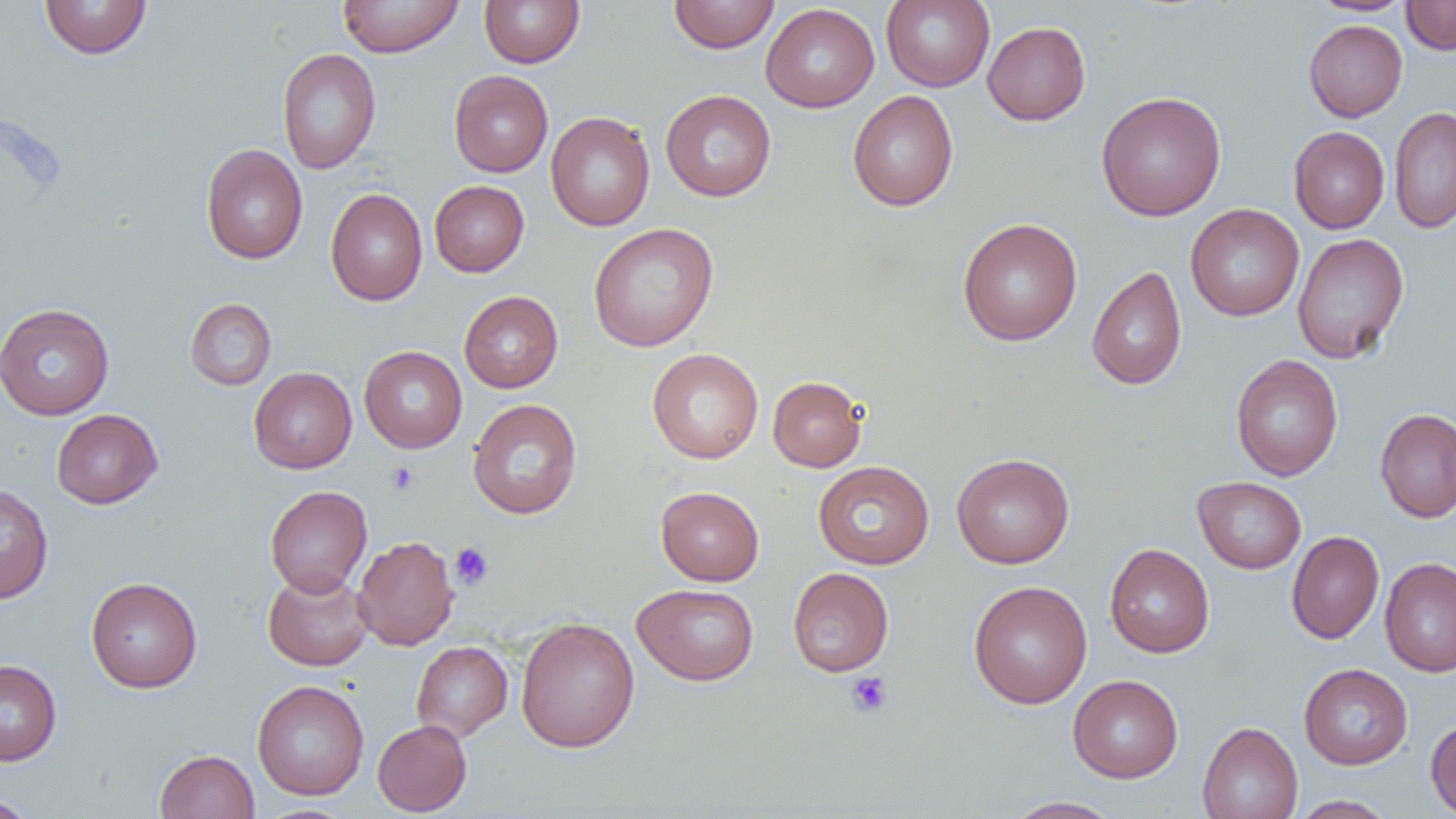

Summary:
  - Coordinate format: approximate bounding boxes as (x1, y1, x2, y2) in pixels
  - Uninfected red blood cell locations: (39, 0, 152, 59), (338, 0, 463, 57), (479, 0, 585, 68), (669, 0, 780, 53), (881, 0, 995, 91), (1308, 0, 1416, 16), (1401, 0, 1456, 55), (761, 3, 880, 112), (1303, 19, 1407, 122), (982, 21, 1091, 126), (277, 48, 381, 174), (448, 70, 553, 177), (660, 90, 776, 202), (848, 90, 959, 211), (1096, 91, 1226, 220), (1389, 106, 1456, 233), (545, 112, 655, 231), (1289, 126, 1390, 234), (201, 144, 308, 264), (429, 180, 529, 276), (325, 188, 427, 305), (1185, 204, 1304, 321), (957, 217, 1083, 346), (588, 223, 719, 352), (1292, 232, 1410, 364), (1087, 266, 1187, 390), (459, 291, 563, 393), (185, 298, 276, 390), (0, 303, 115, 420), (359, 346, 467, 453), (647, 348, 764, 463), (1230, 354, 1343, 481), (248, 367, 357, 473), (768, 375, 866, 472), (467, 398, 582, 519), (1375, 408, 1456, 523), (51, 409, 162, 509), (951, 452, 1075, 569), (813, 460, 934, 569), (1193, 476, 1306, 573), (0, 482, 54, 604), (265, 485, 372, 597), (655, 486, 764, 586), (1286, 530, 1384, 644), (352, 535, 459, 650), (1104, 543, 1214, 658), (1380, 557, 1456, 676), (787, 567, 894, 676), (262, 569, 374, 671), (85, 577, 203, 693), (968, 580, 1092, 708), (632, 583, 759, 686), (515, 617, 640, 753), (411, 641, 512, 742), (0, 659, 62, 766), (1299, 663, 1413, 769), (1068, 675, 1183, 783), (252, 680, 369, 800), (1425, 717, 1456, 818), (372, 719, 472, 816), (1197, 721, 1303, 819), (155, 749, 259, 819), (0, 795, 39, 819), (1290, 795, 1397, 818), (1003, 796, 1123, 818), (253, 804, 358, 819)
  - Platelet locations: (387, 462, 419, 495), (450, 542, 494, 589), (845, 671, 892, 717)
  - Slide-level diagnosis: no evidence of blood parasites
  - Magnification: 1000x
  - Field of view: one of a larger specimen
  - Modality: light microscopy
  - Preparation: thin blood film
  - Image size: 1456×819 pixels